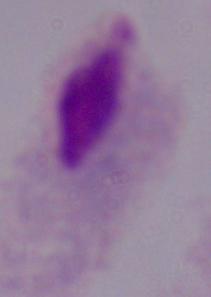
A trichomonad is seen. Captured at 1000x magnification. Micrograph.